Point out each leukocyte.
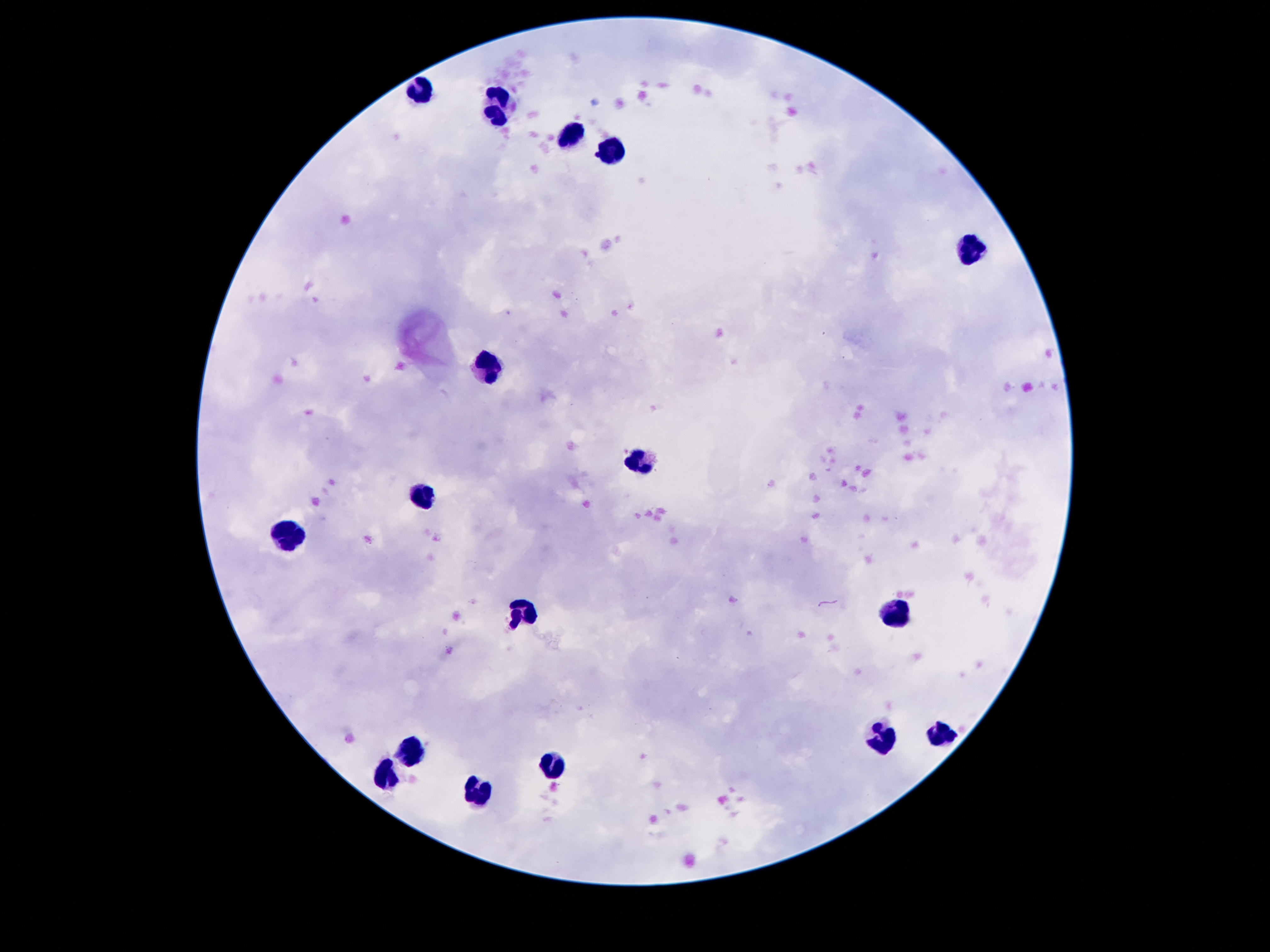

Approximate centers as {x, y} in pixels.
Leukocytes: {421, 91}, {500, 106}, {574, 134}, {610, 152}, {967, 251}, {486, 361}, {645, 463}, {421, 494}, {288, 534}, {530, 612}, {893, 613}, {943, 735}, {880, 737}, {410, 746}, {553, 767}, {385, 773}, {482, 790}.

field_of_view: single
stain: Giemsa
magnification: 100x
preparation: thick blood smear
patient_malaria_status: uninfected
capture: smartphone camera through the microscope eyepiece
image_size: 1270×952 pixels